Name the blood parasite species.
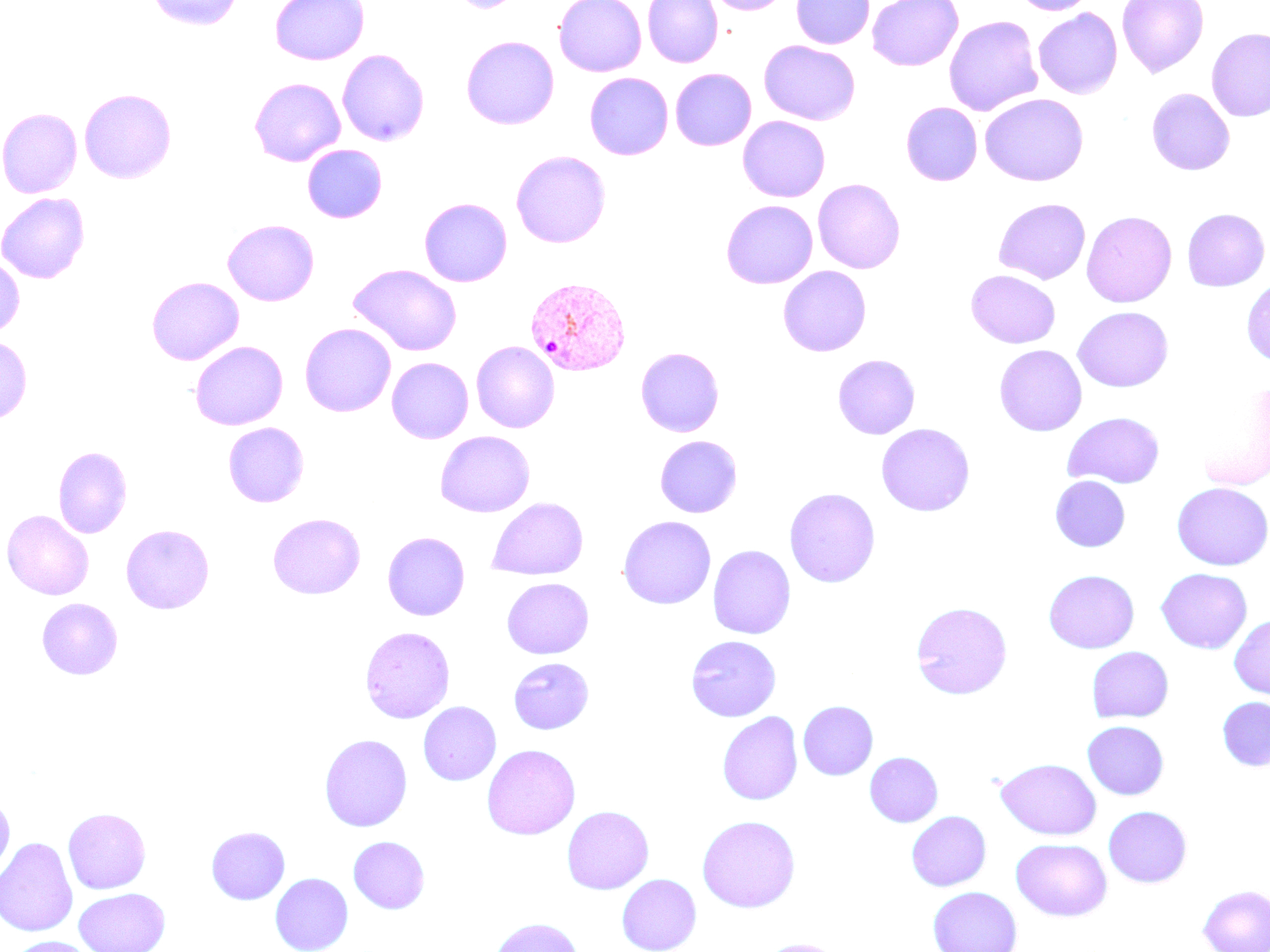

Plasmodium vivax.

Summary:
  - Coordinate format: approximate bounding boxes as [x1, y1, x2, y2] in pixels
  - Plasmodium vivax-infected red blood cell locations: [524, 277, 633, 377], [1241, 277, 1270, 369]
  - Uninfected red blood cell locations: [146, 0, 245, 31], [269, 0, 369, 65], [449, 0, 523, 13], [554, 0, 647, 77], [642, 0, 723, 68], [706, 0, 790, 14], [791, 0, 875, 49], [867, 0, 963, 71], [1011, 0, 1096, 15], [1116, 0, 1209, 78], [1033, 8, 1122, 99], [943, 15, 1043, 116], [1206, 28, 1270, 122], [461, 35, 560, 130], [759, 41, 860, 125], [336, 48, 430, 147], [670, 67, 756, 151], [584, 72, 673, 160], [249, 77, 345, 167], [1146, 87, 1235, 175], [79, 88, 177, 183], [980, 93, 1088, 186], [901, 102, 982, 186], [0, 108, 82, 198], [737, 116, 830, 202], [302, 144, 387, 223], [510, 150, 611, 248], [812, 178, 906, 273], [0, 192, 90, 284], [419, 197, 513, 287], [993, 198, 1090, 284], [720, 200, 818, 289], [1182, 208, 1269, 291], [1081, 210, 1178, 307], [223, 219, 319, 306], [0, 255, 25, 338], [348, 264, 462, 356], [778, 266, 871, 356], [966, 269, 1061, 348], [147, 277, 244, 365], [1072, 306, 1174, 392], [299, 323, 396, 417], [0, 337, 32, 423], [190, 340, 287, 430], [471, 341, 559, 433], [994, 345, 1087, 436], [635, 347, 724, 437], [832, 354, 920, 439], [386, 357, 473, 444], [1194, 381, 1270, 491], [1062, 411, 1166, 488], [222, 422, 309, 507], [876, 423, 975, 517], [435, 430, 535, 517], [655, 436, 742, 517], [53, 446, 133, 538], [1050, 475, 1130, 552], [1171, 482, 1270, 571], [783, 487, 881, 588], [488, 497, 588, 579], [2, 510, 94, 600], [268, 512, 365, 599], [617, 516, 716, 609], [121, 524, 214, 614], [382, 531, 470, 621], [707, 544, 796, 639], [1155, 568, 1252, 653], [1043, 569, 1139, 653], [501, 578, 594, 659], [36, 598, 123, 680], [910, 600, 1013, 700], [1229, 614, 1270, 700], [359, 626, 455, 723], [685, 635, 781, 722], [706, 636, 792, 804], [1086, 647, 1174, 723], [508, 656, 594, 734], [1217, 697, 1270, 771], [798, 700, 878, 780], [417, 701, 502, 786], [717, 711, 803, 805], [1082, 721, 1168, 799], [319, 733, 413, 832], [482, 744, 580, 840], [864, 752, 943, 827], [996, 758, 1101, 840], [0, 791, 15, 885], [561, 805, 654, 894], [1103, 805, 1191, 887], [63, 807, 151, 894], [906, 811, 991, 891], [696, 815, 801, 913], [206, 826, 290, 904], [348, 836, 430, 914], [0, 837, 78, 937], [1011, 838, 1111, 921], [270, 872, 354, 952], [616, 873, 702, 952], [1197, 884, 1270, 952], [928, 886, 1022, 952], [74, 888, 170, 952], [488, 916, 584, 952], [7, 936, 99, 952], [755, 938, 846, 952]
  - Stain: May-Grünwald-Giemsa
  - Field of view: single
  - Magnification: 1000x
  - Modality: optical microscopy
  - Image size: 1270×952 pixels
  - Preparation: thin blood film